Classify this cell by malaria status.
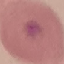

It is uninfected.

Summary:
  - Capture: smartphone through the microscope eyepiece
  - Preparation: thin blood film
  - Image type: automatically extracted cell patch, resized to 64 × 64 pixels
  - Stain: Giemsa